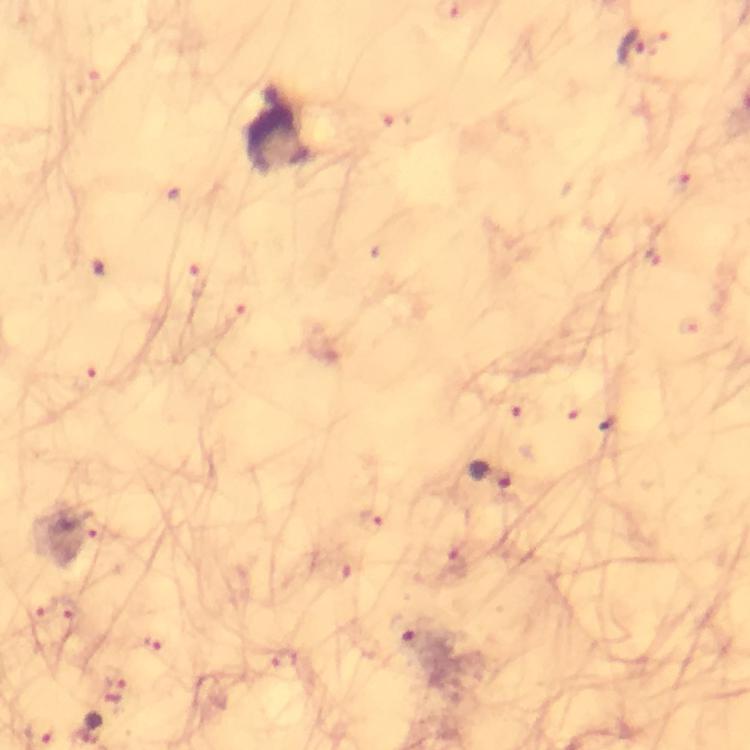

immersion_oil: applied
image_size: 750×750 pixels
context: from a malaria diagnostic workup
magnification: 100x
stain: Giemsa
malaria_parasite_locations: 'approximate centers as [x, y] in pixels: [632, 45], [679, 180], [195, 278], [238, 313], [83, 379], [524, 414], [491, 474], [371, 521], [87, 526], [347, 572], [69, 610], [36, 613], [406, 625], [154, 643], [286, 661], [116, 687], [89, 727], [41, 732]'
cropped_from: a single field of view
capture: smartphone mounted on the microscope
preparation: thick blood film